Point out each malaria parasite.
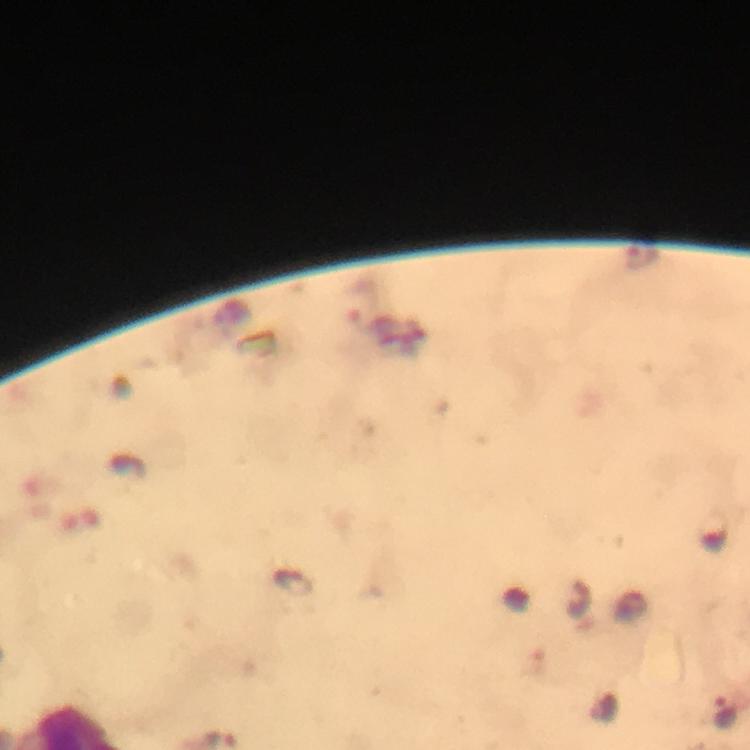
Approximate centers as [x, y] in pixels.
Malaria parasites: [293, 583], [725, 713].

Summary:
  - Cropped from: a single field of view
  - Image size: 750×750 pixels
  - Immersion oil: applied
  - Preparation: thick smear
  - Magnification: 100x
  - Capture: smartphone photograph through a microscope
  - Stain: Giemsa
  - Context: from a malaria diagnostic workup